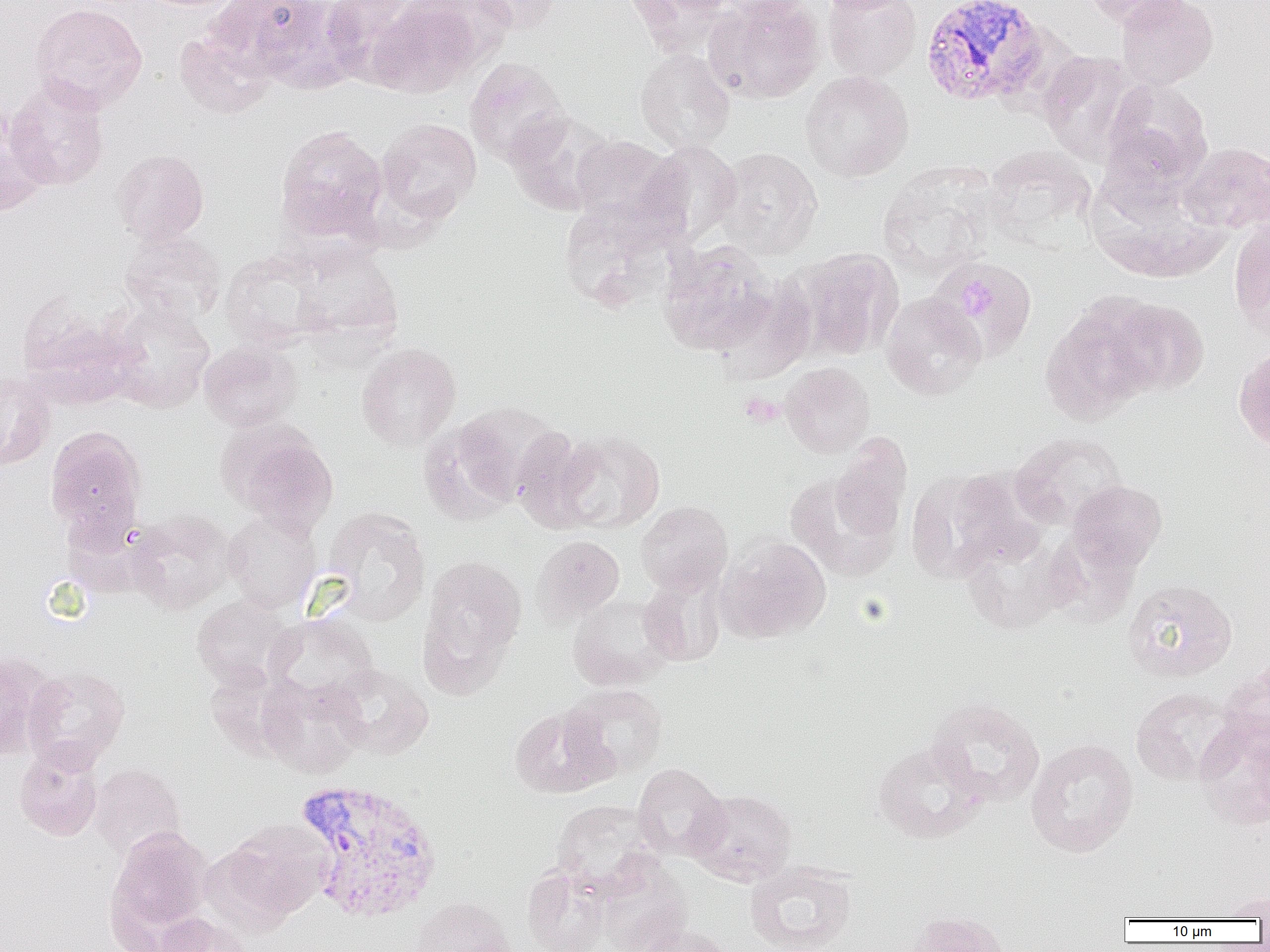

Approximate bounding boxes as [x1, y1, x2, y2] in pixels. Plasmodium vivax-infected red blood cell locations: [921, 0, 1052, 109], [293, 778, 445, 924]. Uninfected red blood cell locations: [211, 0, 342, 87], [320, 0, 422, 85], [405, 0, 516, 71], [471, 0, 563, 34], [623, 0, 737, 56], [705, 0, 825, 104], [716, 0, 815, 23], [818, 0, 911, 14], [822, 0, 922, 82], [1085, 0, 1188, 30], [1116, 0, 1218, 90], [367, 1, 481, 97], [30, 3, 147, 113], [174, 27, 277, 119], [635, 49, 735, 154], [1037, 51, 1142, 165], [465, 58, 570, 168], [800, 70, 914, 182], [4, 77, 110, 191], [1100, 77, 1213, 189], [0, 110, 51, 217], [505, 110, 616, 215], [376, 118, 481, 223], [275, 124, 388, 243], [569, 135, 682, 232], [638, 141, 743, 246], [1180, 142, 1269, 233], [981, 145, 1096, 247], [716, 147, 823, 259], [113, 149, 209, 245], [877, 164, 997, 279], [557, 196, 686, 312], [1229, 219, 1270, 340], [119, 231, 227, 324], [658, 241, 780, 356], [292, 246, 403, 345], [793, 247, 903, 361], [221, 252, 330, 350], [937, 257, 1038, 360], [881, 292, 986, 401], [15, 293, 140, 407], [102, 297, 216, 412], [1104, 297, 1209, 396], [1039, 303, 1158, 425], [199, 339, 303, 432], [356, 342, 461, 450], [1234, 343, 1270, 454], [780, 362, 874, 458], [0, 372, 55, 470], [442, 405, 559, 512], [217, 419, 339, 534], [45, 425, 147, 540], [511, 426, 600, 532], [552, 430, 665, 535], [1010, 432, 1127, 529], [830, 435, 913, 543], [908, 468, 1035, 581], [785, 471, 903, 581], [1066, 480, 1167, 574], [636, 501, 733, 595], [323, 507, 431, 626], [128, 509, 238, 614], [223, 509, 322, 613], [531, 534, 625, 626], [960, 534, 1066, 634], [718, 536, 832, 643], [419, 554, 527, 684], [638, 573, 726, 667], [1122, 578, 1237, 682], [567, 594, 676, 690], [191, 595, 299, 689], [265, 614, 378, 705], [0, 651, 49, 761], [331, 663, 433, 759], [1218, 664, 1270, 758], [22, 666, 130, 772], [256, 674, 370, 778], [560, 683, 667, 781], [1130, 687, 1238, 786], [926, 696, 1045, 806], [509, 706, 614, 799], [1194, 719, 1270, 830], [1026, 738, 1138, 857], [872, 739, 988, 843], [14, 748, 103, 841], [89, 763, 186, 860], [632, 763, 729, 861], [687, 788, 796, 886], [551, 799, 661, 895], [218, 819, 330, 924], [104, 826, 213, 946], [595, 858, 692, 952], [744, 860, 857, 952], [522, 866, 611, 952], [1213, 889, 1270, 921], [407, 895, 517, 952], [903, 910, 1013, 952], [153, 912, 252, 952], [633, 923, 733, 952]. Platelet locations: [943, 258, 1030, 357], [956, 279, 997, 324], [739, 392, 784, 426]. Slide-level diagnosis: Plasmodium vivax. Thin blood smear. Captured at 1000x magnification. Image is 1270×952 pixels. Light microscopy. One field of a larger specimen.